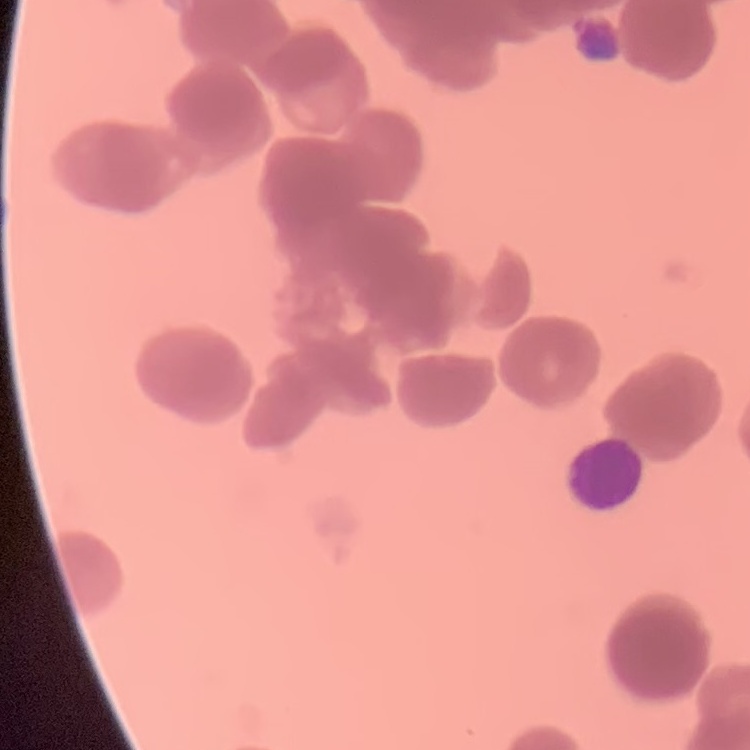
erythrocyte morphology = rouleaux formation
preparation = thin blood film
image type = square crop of a larger photomicrograph
stain = Field's or Giemsa